Identify the cell.
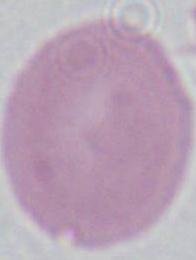
An erythrocyte.

Micrograph. Captured at 1000x magnification.